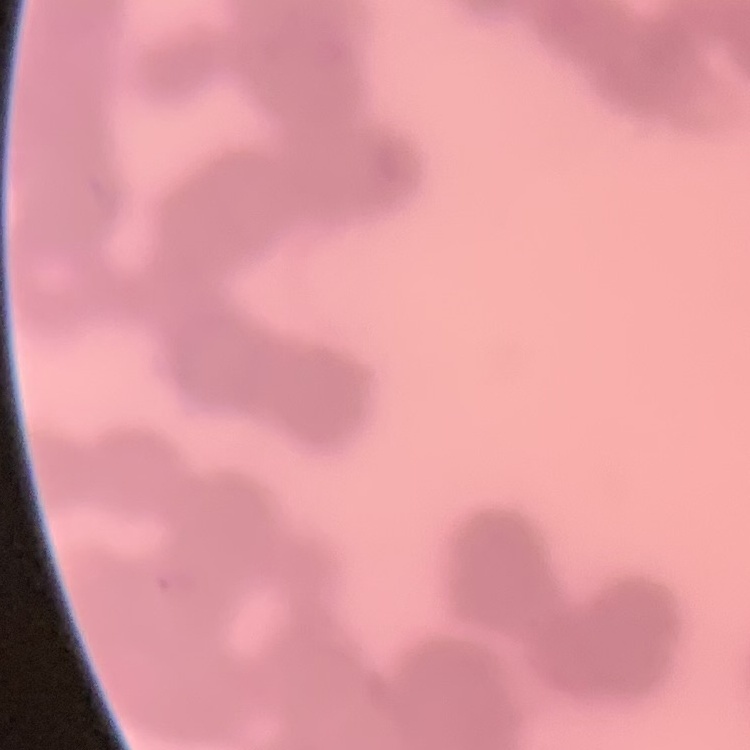

{
  "red_blood_cell_morphology": "rouleaux formation",
  "preparation": "thin peripheral smear",
  "stain": "Field's or Giemsa",
  "image_type": "one tile cut from a larger photomicrograph"
}